Assess the morphology of the erythrocytes.
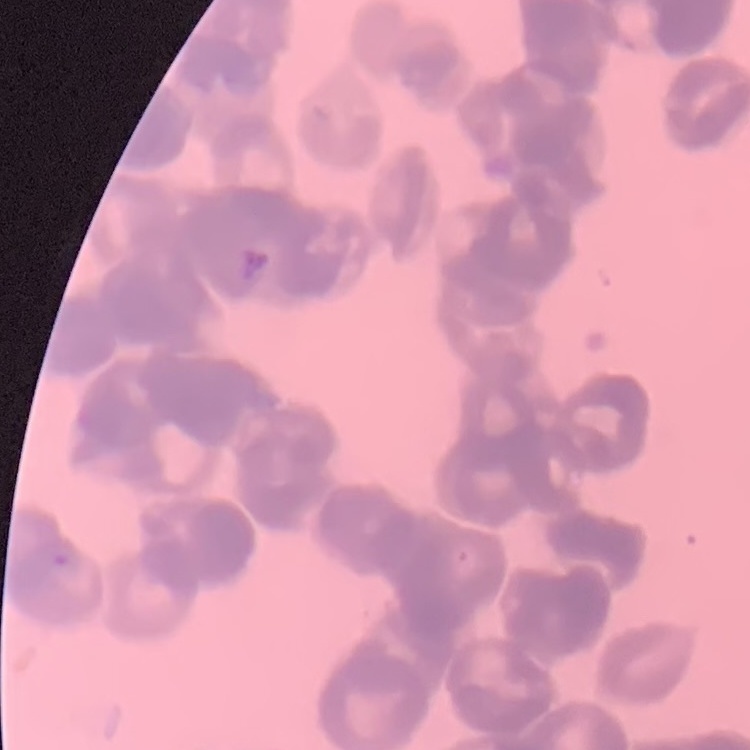
Rouleaux formation.

preparation = thin blood smear
stain = Field's or Giemsa
image type = one tile cut from a larger photomicrograph